Classify this cell by malaria status.
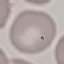
Uninfected.

Automatically extracted cell patch, resized to 64 × 64 pixels. Giemsa stain. Thin smear of blood. Photographed with a smartphone camera at the microscope eyepiece.